Comment on the morphology of the erythrocytes.
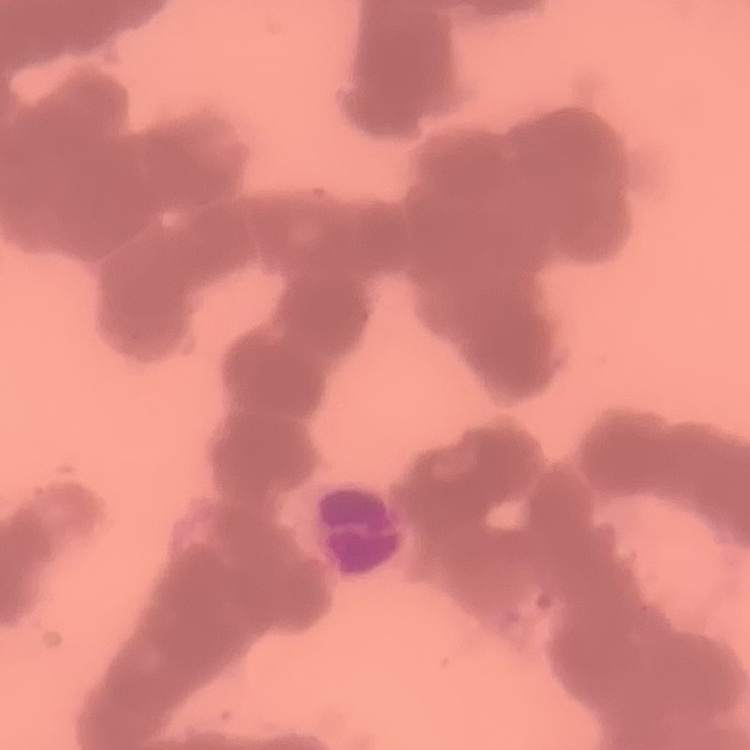

Rouleaux formation.

Square crop of a larger photomicrograph. Thin peripheral smear. Field's or Giemsa stain.